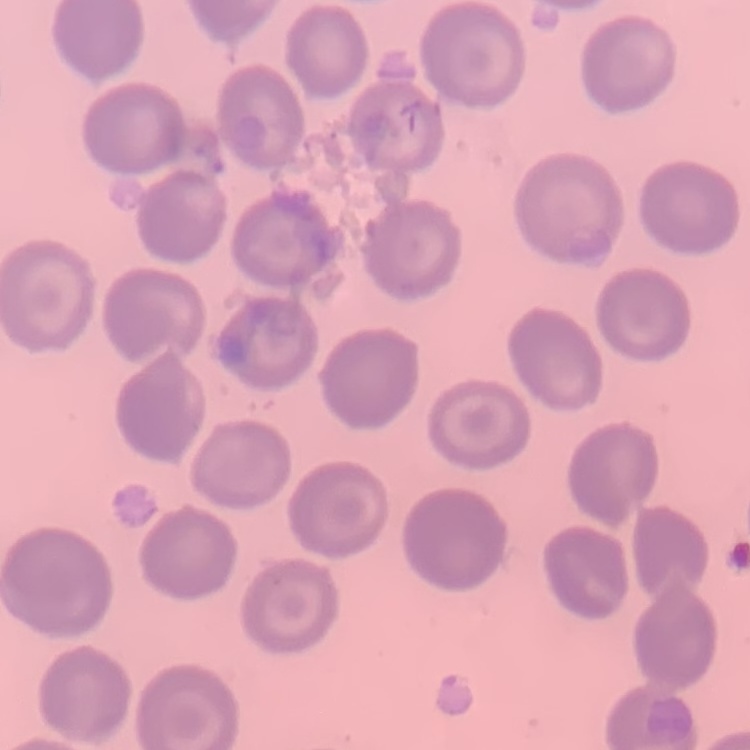

erythrocyte morphology = no rouleaux formation
image type = one tile cut from a larger photomicrograph
preparation = thin blood smear
stain = Field's or Giemsa